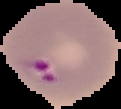
Result: Plasmodium parasites identified. Image is 121×109 pixels. Cell region segmented out of the field of view; the surrounding area is masked to black. From a thin blood film.